State which parasite is depicted.
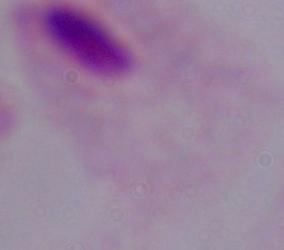
This is a trichomonad.

Summary:
  - Modality: photomicrograph
  - Magnification: 1000x